Report the malaria status of this cell.
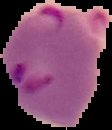
It is parasitized.

From a thin blood film. Image is 112×130 pixels. Segmented cell region on a black background.